Classify this cell by malaria status.
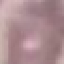
Uninfected.

{
  "stain": "Giemsa",
  "capture": "smartphone through the microscope eyepiece",
  "preparation": "thin smear",
  "image_type": "cell patch, automatically extracted from a larger field of view and resized to 64 × 64 pixels"
}